Outline each blood parasite and name the species.
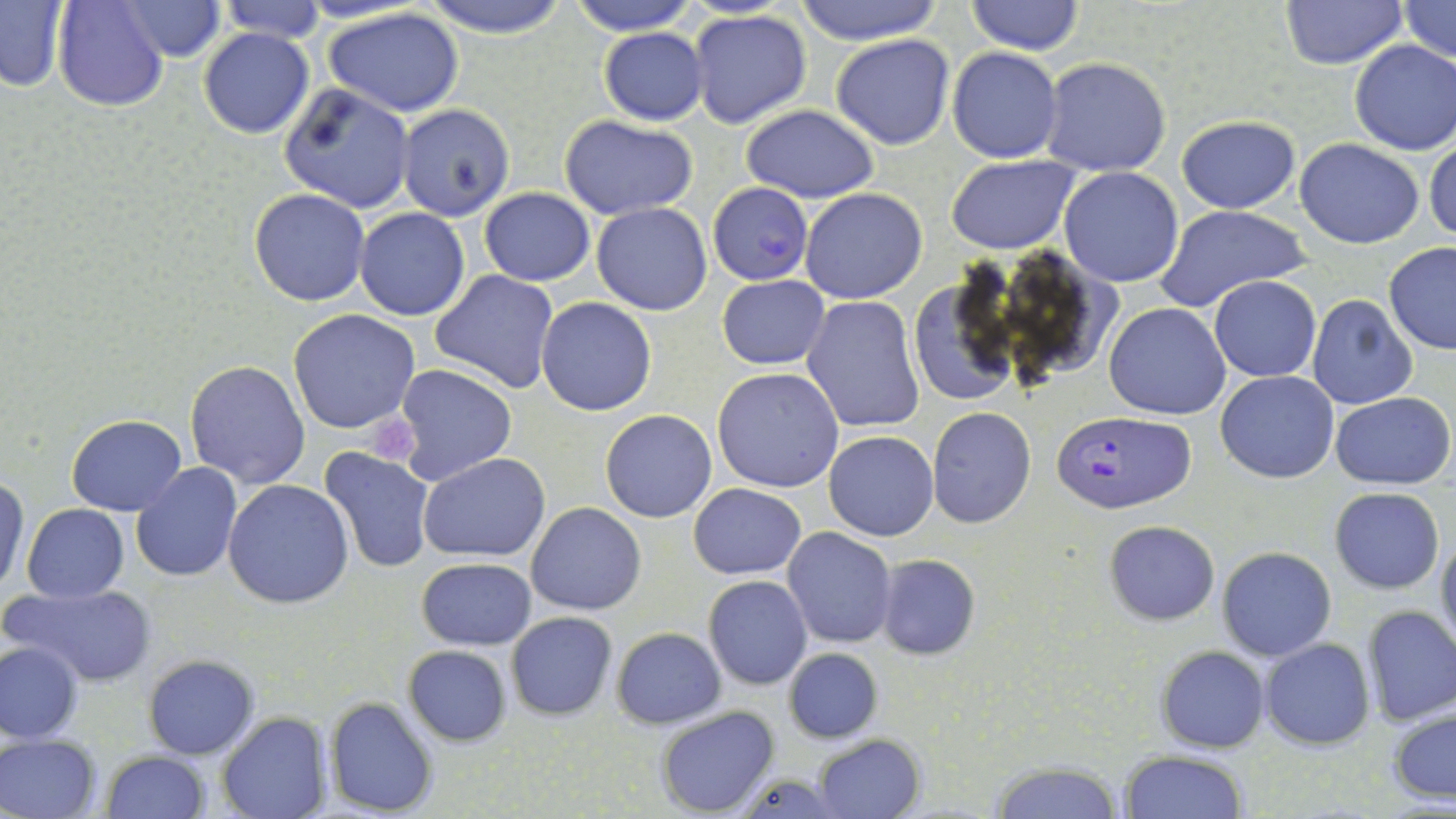

Approximate bounding boxes as named x1/y1/x2/y2 corners in pixels.
Plasmodium falciparum-infected red blood cells: (x1=708, y1=182, x2=814, y2=286), (x1=1048, y1=410, x2=1197, y2=515).
No Plasmodium ovale, Plasmodium malariae, Plasmodium vivax, Babesia divergens, or Trypanosoma brucei observed.

Uninfected red blood cell locations: (x1=54, y1=0, x2=169, y2=112), (x1=118, y1=0, x2=227, y2=61), (x1=215, y1=0, x2=327, y2=44), (x1=418, y1=0, x2=572, y2=39), (x1=567, y1=0, x2=698, y2=35), (x1=789, y1=0, x2=946, y2=45), (x1=965, y1=0, x2=1083, y2=55), (x1=1278, y1=0, x2=1407, y2=69), (x1=1396, y1=0, x2=1455, y2=65), (x1=0, y1=2, x2=69, y2=90), (x1=321, y1=6, x2=467, y2=116), (x1=688, y1=9, x2=814, y2=130), (x1=198, y1=26, x2=314, y2=140), (x1=598, y1=28, x2=708, y2=126), (x1=830, y1=34, x2=955, y2=150), (x1=1349, y1=39, x2=1456, y2=156), (x1=947, y1=47, x2=1063, y2=163), (x1=1040, y1=57, x2=1172, y2=176), (x1=278, y1=82, x2=416, y2=211), (x1=398, y1=104, x2=516, y2=222), (x1=739, y1=105, x2=881, y2=201), (x1=1177, y1=115, x2=1302, y2=214), (x1=559, y1=117, x2=700, y2=218), (x1=1295, y1=139, x2=1424, y2=249), (x1=1425, y1=140, x2=1456, y2=242), (x1=947, y1=154, x2=1080, y2=254), (x1=1059, y1=167, x2=1184, y2=287), (x1=479, y1=187, x2=595, y2=286), (x1=249, y1=188, x2=371, y2=307), (x1=800, y1=188, x2=929, y2=304), (x1=590, y1=203, x2=712, y2=316), (x1=1155, y1=204, x2=1308, y2=316), (x1=354, y1=207, x2=470, y2=321), (x1=1383, y1=242, x2=1456, y2=353), (x1=430, y1=269, x2=561, y2=394), (x1=906, y1=272, x2=1022, y2=409), (x1=717, y1=275, x2=830, y2=369), (x1=1209, y1=276, x2=1322, y2=383), (x1=1306, y1=293, x2=1418, y2=410), (x1=802, y1=295, x2=924, y2=433), (x1=535, y1=297, x2=658, y2=416), (x1=1105, y1=302, x2=1231, y2=420), (x1=288, y1=309, x2=421, y2=433), (x1=185, y1=360, x2=311, y2=488), (x1=394, y1=364, x2=518, y2=485), (x1=712, y1=367, x2=844, y2=493), (x1=1215, y1=369, x2=1340, y2=485), (x1=1329, y1=392, x2=1455, y2=487), (x1=926, y1=406, x2=1036, y2=528), (x1=600, y1=409, x2=716, y2=523), (x1=67, y1=413, x2=187, y2=515), (x1=824, y1=431, x2=939, y2=541), (x1=321, y1=447, x2=435, y2=573), (x1=418, y1=453, x2=551, y2=562), (x1=130, y1=462, x2=244, y2=582), (x1=0, y1=475, x2=27, y2=595), (x1=223, y1=479, x2=354, y2=609), (x1=689, y1=482, x2=807, y2=579), (x1=1330, y1=487, x2=1444, y2=593), (x1=526, y1=501, x2=646, y2=615), (x1=22, y1=504, x2=129, y2=603), (x1=1103, y1=519, x2=1221, y2=624), (x1=783, y1=527, x2=897, y2=648), (x1=1436, y1=529, x2=1456, y2=656), (x1=1216, y1=547, x2=1337, y2=662), (x1=874, y1=553, x2=981, y2=660), (x1=416, y1=557, x2=538, y2=650), (x1=702, y1=575, x2=813, y2=691), (x1=8, y1=582, x2=158, y2=688), (x1=1360, y1=605, x2=1456, y2=726), (x1=506, y1=610, x2=617, y2=718), (x1=610, y1=626, x2=726, y2=729), (x1=1260, y1=637, x2=1375, y2=749), (x1=1, y1=639, x2=85, y2=743), (x1=402, y1=644, x2=513, y2=746), (x1=1156, y1=645, x2=1269, y2=752), (x1=783, y1=648, x2=882, y2=743), (x1=144, y1=654, x2=259, y2=758), (x1=324, y1=696, x2=439, y2=817), (x1=1387, y1=704, x2=1455, y2=808), (x1=656, y1=705, x2=780, y2=817), (x1=217, y1=713, x2=330, y2=819), (x1=0, y1=734, x2=102, y2=819), (x1=813, y1=734, x2=925, y2=819), (x1=1119, y1=749, x2=1248, y2=819), (x1=99, y1=750, x2=210, y2=818), (x1=987, y1=759, x2=1125, y2=819), (x1=730, y1=769, x2=838, y2=817). Platelet locations: (x1=361, y1=416, x2=419, y2=465). Slide-level diagnosis: Plasmodium falciparum. May-Grünwald-Giemsa stain. Single field of view. Thin blood smear. Light microscopy. Image is 1456×819 pixels. 1000x magnification.